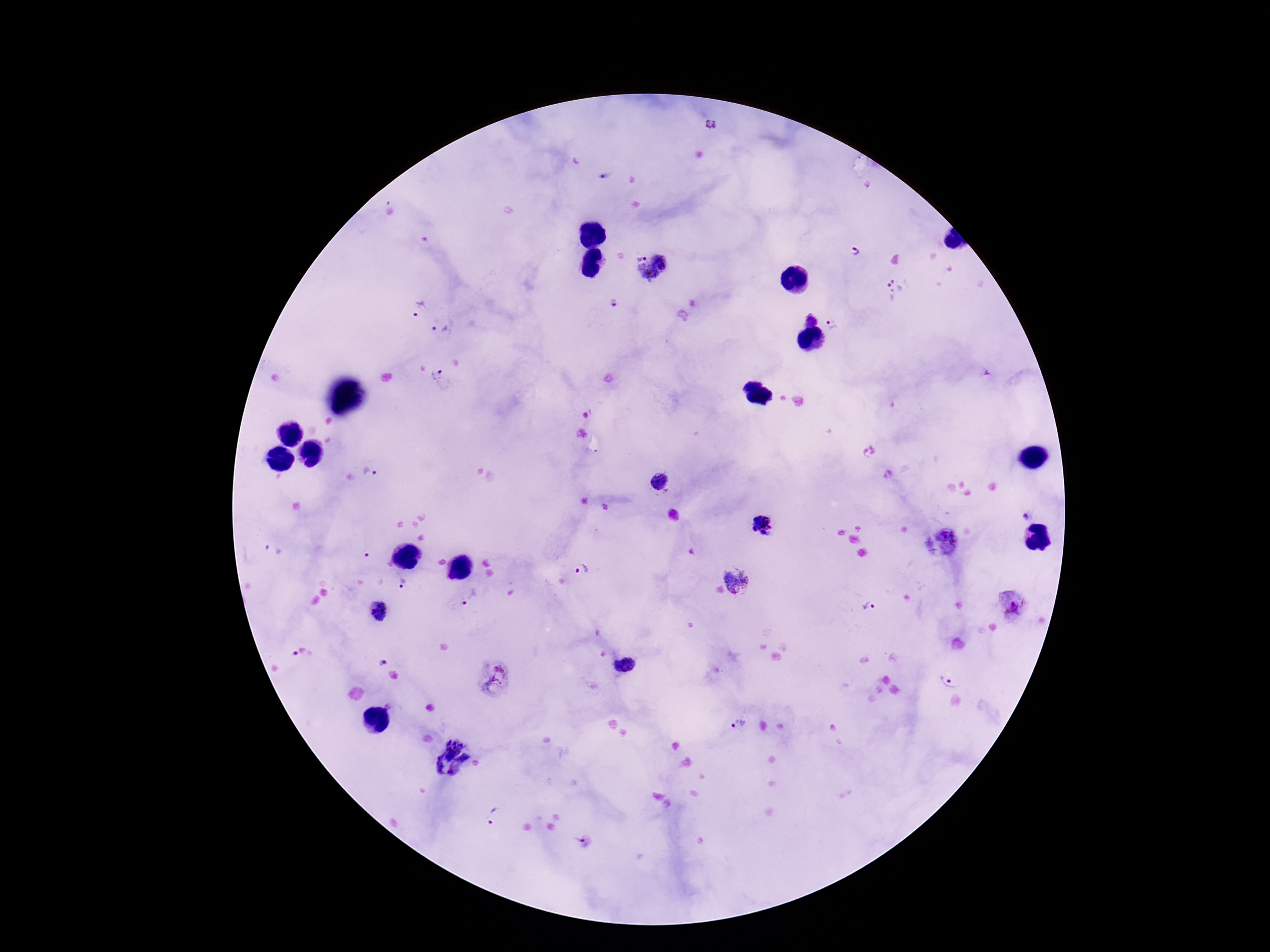
capture: smartphone camera through the microscope eyepiece
stain: Giemsa
magnification: 100x
patient_malaria_status: positive
field_of_view: one from this slide
preparation: thick peripheral-blood smear
plasmodium_parasite_locations: 'approximate centers as [x, y] in pixels: [709, 125], [604, 177], [856, 250], [639, 254], [662, 258], [647, 274], [893, 289], [612, 303], [417, 307], [811, 318], [834, 324], [439, 330], [443, 381], [370, 473], [658, 483], [1026, 515], [761, 524], [940, 541], [581, 570], [738, 580], [404, 582], [471, 598], [1015, 605], [867, 606], [379, 610], [383, 662], [630, 664], [612, 667], [492, 677], [949, 677], [739, 723], [448, 757], [492, 815], [586, 842]'
image_size: 1270×952 pixels